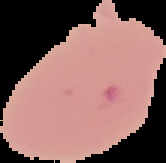

result = no Plasmodium parasites seen
image size = 166×163 pixels
preparation = thin blood smear
image type = segmented cell region with the area outside set to black